Identify the parasite.
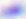
This is Toxoplasma gondii.

{
  "magnification": "400x",
  "modality": "micrograph"
}